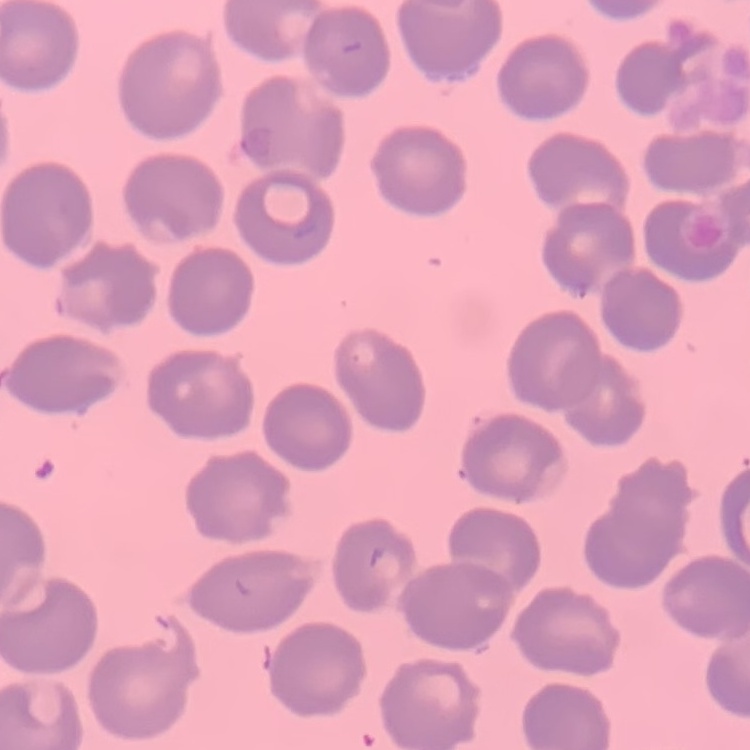 The erythrocytes show no rouleaux formation. Thin blood smear. Stained with either Field's or Giemsa. One tile cut from a larger photomicrograph.